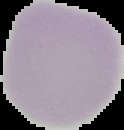

Cell region segmented out of the field of view; the surrounding area is masked to black. From a thin blood film. Image is 124×130 pixels. Malaria status: uninfected.